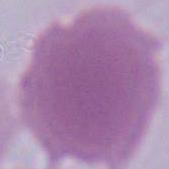 Photomicrograph. 1000x magnification. A red blood cell is seen.